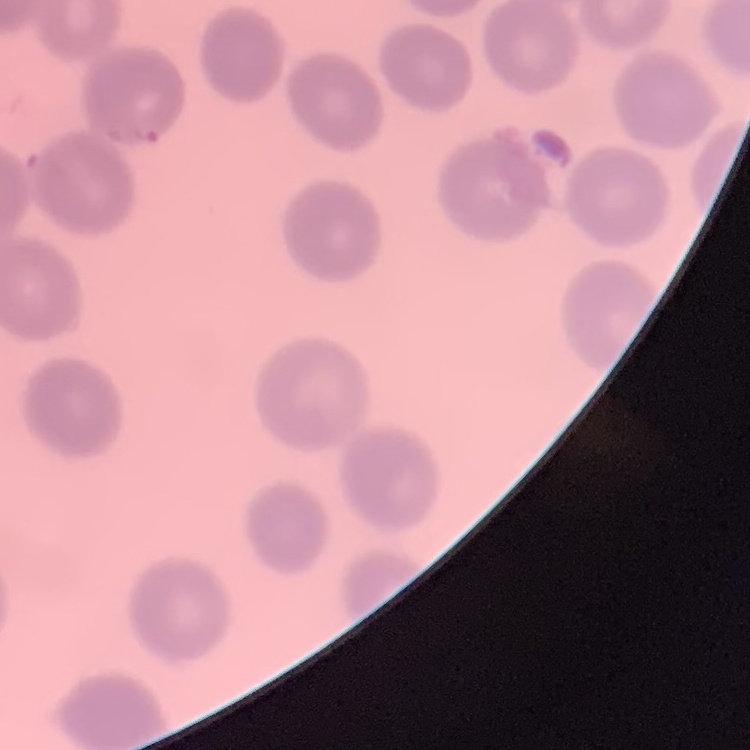

{
  "erythrocyte_morphology": "no rouleaux formation",
  "image_type": "one tile cut from a larger photomicrograph",
  "stain": "Field's or Giemsa",
  "preparation": "thin blood smear"
}